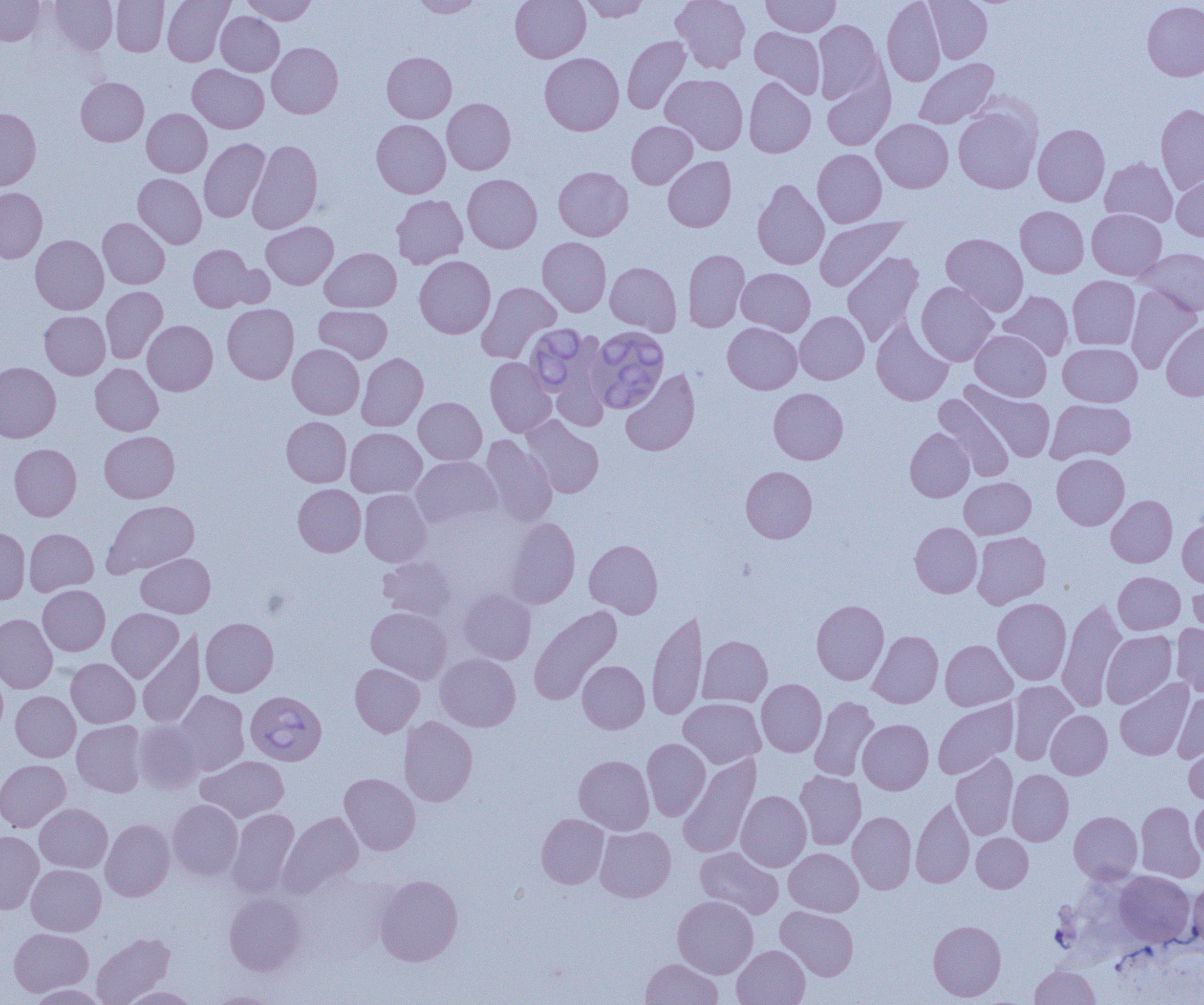

Babesia divergens-infected red blood cell locations = approximate bounding boxes as [x1, y1, x2, y2] in pixels: [524, 324, 591, 395], [588, 329, 671, 413], [244, 694, 330, 767]
slide-level diagnosis = Babesia divergens
uninfected red blood cell locations = approximate bounding boxes as [x1, y1, x2, y2] in pixels: [0, 0, 45, 45], [50, 0, 118, 55], [111, 0, 169, 56], [162, 0, 234, 66], [241, 0, 317, 25], [412, 0, 485, 18], [510, 0, 590, 62], [579, 0, 650, 22], [670, 0, 750, 73], [762, 0, 841, 36], [882, 0, 946, 86], [924, 0, 993, 63], [1142, 1, 1204, 81], [216, 11, 284, 76], [813, 19, 884, 104], [750, 27, 826, 98], [621, 36, 691, 114], [267, 42, 343, 118], [382, 52, 457, 123], [539, 53, 624, 136], [914, 58, 999, 129], [187, 64, 268, 133], [660, 74, 748, 155], [822, 74, 894, 151], [76, 77, 149, 146], [744, 77, 816, 158], [442, 98, 516, 174], [1155, 104, 1204, 194], [953, 105, 1042, 193], [0, 107, 41, 191], [142, 108, 212, 177], [872, 118, 953, 192], [371, 119, 450, 198], [626, 121, 698, 189], [1033, 123, 1110, 207], [199, 138, 270, 222], [248, 139, 323, 233], [812, 149, 887, 227], [663, 156, 736, 232], [1100, 158, 1178, 227], [553, 166, 633, 241], [133, 173, 207, 248], [1171, 173, 1204, 241], [462, 174, 542, 253], [752, 179, 829, 270], [0, 187, 47, 264], [391, 194, 468, 269], [1015, 205, 1089, 278], [1087, 209, 1166, 280], [814, 217, 906, 291], [98, 218, 170, 289], [261, 222, 338, 289], [941, 233, 1028, 316], [30, 234, 108, 314], [537, 236, 611, 316], [188, 244, 255, 312], [320, 248, 401, 312], [1135, 248, 1204, 316], [683, 249, 750, 332], [841, 251, 924, 347], [414, 256, 495, 339], [605, 262, 682, 336], [225, 264, 274, 308], [736, 267, 815, 336], [1067, 275, 1140, 350], [476, 282, 561, 363], [916, 282, 999, 366], [1125, 285, 1201, 373], [101, 286, 167, 364], [999, 291, 1074, 360], [223, 303, 299, 384], [315, 305, 392, 362], [40, 311, 110, 379], [795, 311, 869, 384], [871, 318, 954, 406], [142, 320, 217, 396], [1161, 321, 1204, 401], [722, 322, 802, 394], [970, 329, 1051, 401], [549, 334, 611, 430], [1058, 342, 1142, 406], [288, 344, 365, 419], [357, 353, 428, 431], [485, 357, 556, 437], [0, 362, 61, 442], [90, 363, 163, 436], [620, 368, 700, 456], [960, 381, 1056, 462], [768, 388, 848, 464], [933, 393, 1014, 481], [414, 397, 487, 464], [1046, 399, 1136, 464], [521, 416, 604, 498], [281, 417, 351, 487], [345, 427, 426, 498], [905, 427, 974, 502], [99, 431, 179, 503], [480, 434, 557, 527], [9, 443, 81, 520], [1052, 453, 1129, 529], [411, 456, 501, 529], [741, 466, 817, 543], [959, 477, 1036, 539], [293, 484, 366, 556], [359, 489, 432, 566], [1106, 495, 1177, 567], [101, 500, 199, 578], [506, 518, 580, 608], [1178, 518, 1204, 587], [910, 522, 982, 598], [0, 527, 30, 604], [25, 528, 98, 596], [972, 532, 1051, 609], [584, 539, 663, 618], [136, 553, 214, 617], [379, 556, 457, 622], [1113, 571, 1185, 634], [1187, 574, 1204, 641], [37, 585, 110, 655], [459, 588, 536, 665], [993, 598, 1071, 685], [811, 599, 889, 685], [1056, 599, 1127, 712], [529, 605, 623, 705], [366, 607, 451, 683], [107, 608, 183, 682], [647, 609, 708, 721], [0, 613, 58, 693], [200, 617, 278, 697], [1171, 623, 1204, 697], [137, 630, 205, 728], [867, 630, 943, 708], [1101, 630, 1177, 708], [698, 635, 772, 707], [940, 639, 1017, 710], [435, 653, 520, 731], [66, 658, 140, 728], [578, 660, 650, 733], [350, 663, 424, 737], [0, 666, 8, 740], [1115, 678, 1194, 760], [756, 679, 827, 757], [1008, 680, 1078, 765], [173, 690, 249, 776], [1173, 690, 1204, 762], [10, 691, 80, 762], [809, 696, 879, 781], [679, 697, 765, 768], [933, 698, 1018, 779], [1046, 710, 1112, 779], [399, 716, 478, 806], [858, 719, 933, 794], [72, 720, 147, 797], [133, 720, 203, 794], [641, 738, 711, 821], [1184, 740, 1204, 805], [678, 753, 761, 859], [950, 753, 1018, 840], [197, 755, 289, 822], [574, 755, 654, 835], [0, 759, 71, 832], [1007, 769, 1073, 846], [794, 770, 867, 850], [339, 773, 421, 855], [736, 790, 811, 872], [1191, 796, 1204, 865], [911, 798, 975, 888], [167, 799, 243, 880], [1135, 801, 1204, 882], [34, 802, 112, 873], [227, 808, 300, 898], [278, 811, 364, 897], [848, 811, 916, 893], [1069, 811, 1142, 883], [536, 813, 609, 888], [100, 818, 175, 901], [595, 826, 676, 902], [0, 830, 44, 914], [971, 833, 1033, 892], [695, 846, 784, 919], [784, 847, 863, 916], [26, 864, 106, 936], [1114, 871, 1195, 947], [374, 874, 463, 966], [1187, 880, 1204, 951], [224, 892, 306, 975], [672, 895, 758, 978], [775, 906, 858, 980], [928, 920, 1006, 1001], [9, 928, 92, 997], [91, 932, 175, 1005], [732, 945, 810, 1005], [640, 958, 723, 1005], [1029, 965, 1100, 1005], [27, 984, 108, 1004], [119, 986, 200, 1004], [204, 991, 281, 1004]
modality = optical microscopy
preparation = thin blood smear
magnification = 1000x
field of view = single
image size = 1204×1005 pixels